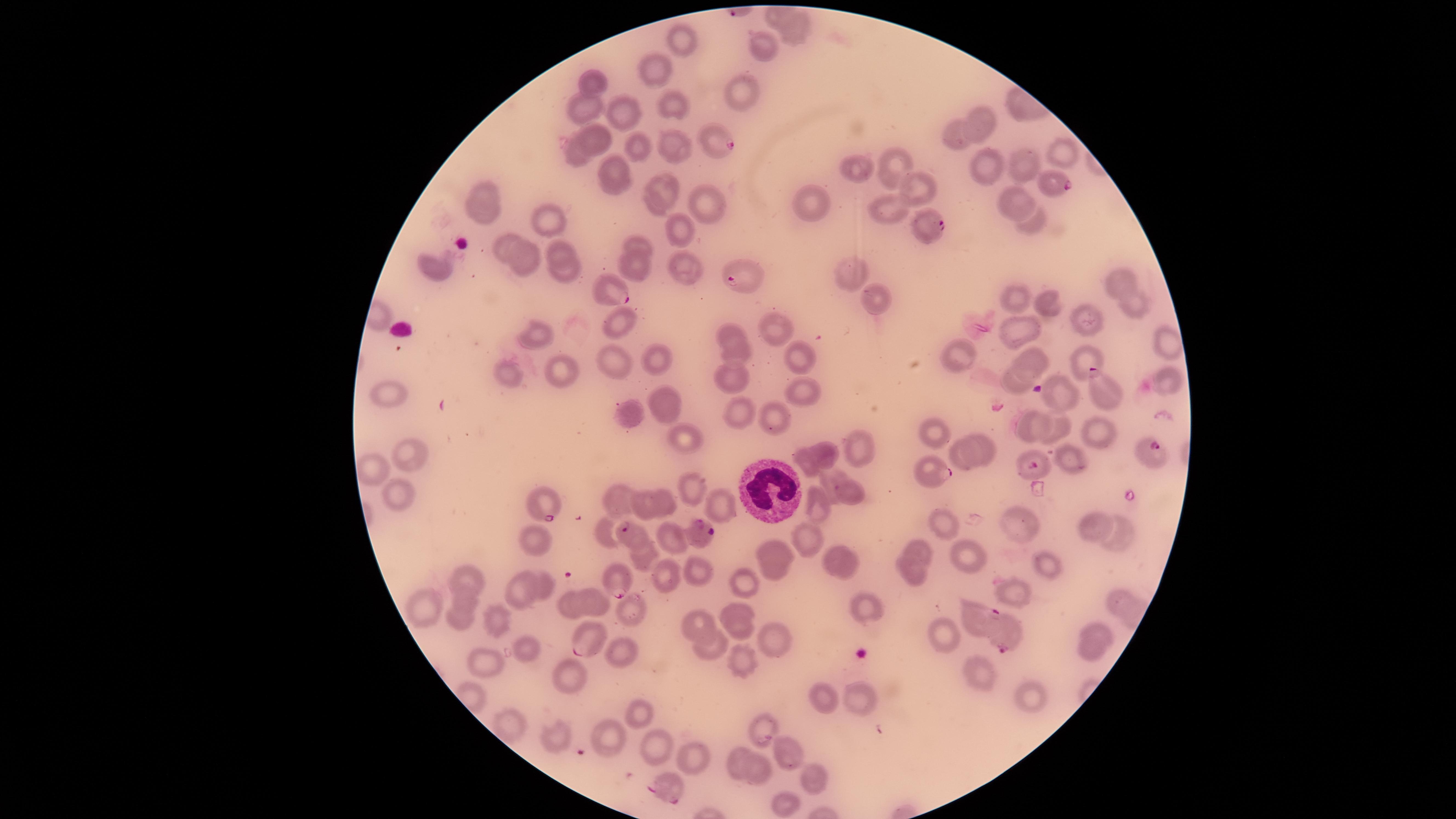

{
  "image_size": "1456×819 pixels",
  "visible_region": "circular",
  "presence": "malaria parasites seen",
  "parasitized_RBCs": "approximate marker points as [x, y] in pixels: [718, 144], [1056, 185], [926, 226], [741, 278], [607, 290], [1102, 392], [1155, 454], [1033, 465], [932, 475], [540, 505], [631, 534], [700, 535], [619, 580], [971, 616], [1006, 635], [584, 638], [669, 789]",
  "stain": "Giemsa",
  "uninfected_RBCs": "approximate marker points as [x, y] in pixels: [798, 35], [678, 41], [762, 47], [650, 72], [591, 86], [739, 95], [587, 107], [671, 107], [624, 113], [981, 123], [957, 136], [599, 139], [635, 147], [672, 147], [1066, 153], [578, 154], [1023, 162], [900, 167], [986, 167], [860, 171], [615, 173], [919, 188], [666, 189], [487, 192], [1009, 198], [704, 201], [812, 203], [654, 205], [890, 208], [483, 215], [548, 218], [1031, 224], [680, 230], [637, 244], [501, 248], [435, 265], [523, 265], [636, 266], [685, 270], [850, 273], [1118, 282], [874, 302], [1137, 302], [1013, 303], [1049, 306], [620, 323], [1088, 323], [780, 328], [1019, 332], [540, 336], [733, 336], [1166, 341], [657, 355], [735, 356], [799, 357], [959, 358], [1039, 360], [1082, 360], [620, 365], [564, 370], [515, 376], [732, 376], [1015, 381], [1163, 385], [1060, 392], [391, 394], [804, 394], [657, 403], [630, 414], [741, 414], [774, 416], [679, 435], [410, 444], [858, 447], [827, 453], [803, 464], [374, 467], [830, 477], [695, 490], [394, 494], [851, 495], [721, 502], [623, 503], [666, 503], [642, 506], [819, 511], [940, 521], [1016, 523], [1093, 524], [602, 531], [1123, 531], [673, 535], [537, 540], [809, 541], [775, 548], [914, 551], [968, 556], [642, 557], [832, 557], [1046, 566], [852, 568], [663, 573], [701, 574], [772, 574], [914, 576], [544, 578], [466, 579], [746, 582], [518, 590], [1014, 592], [589, 594], [1119, 597], [465, 600], [423, 606], [861, 606], [739, 609], [569, 610], [631, 614], [457, 618], [500, 619], [700, 623], [742, 629], [1099, 631], [939, 637], [777, 642], [525, 648], [714, 649], [623, 651], [1089, 655], [743, 662], [488, 666], [976, 675], [566, 677], [861, 697], [1027, 698], [824, 699], [639, 710], [765, 728], [509, 730], [608, 739], [555, 741], [656, 749], [788, 752], [691, 759], [735, 759], [757, 773], [815, 784], [783, 810]",
  "species": "Plasmodium falciparum",
  "preparation": "thin blood film",
  "capture": "smartphone photograph through the microscope eyepiece",
  "WBCs": "approximate marker points as [x, y] in pixels: [767, 490]",
  "field_of_view": "single"
}